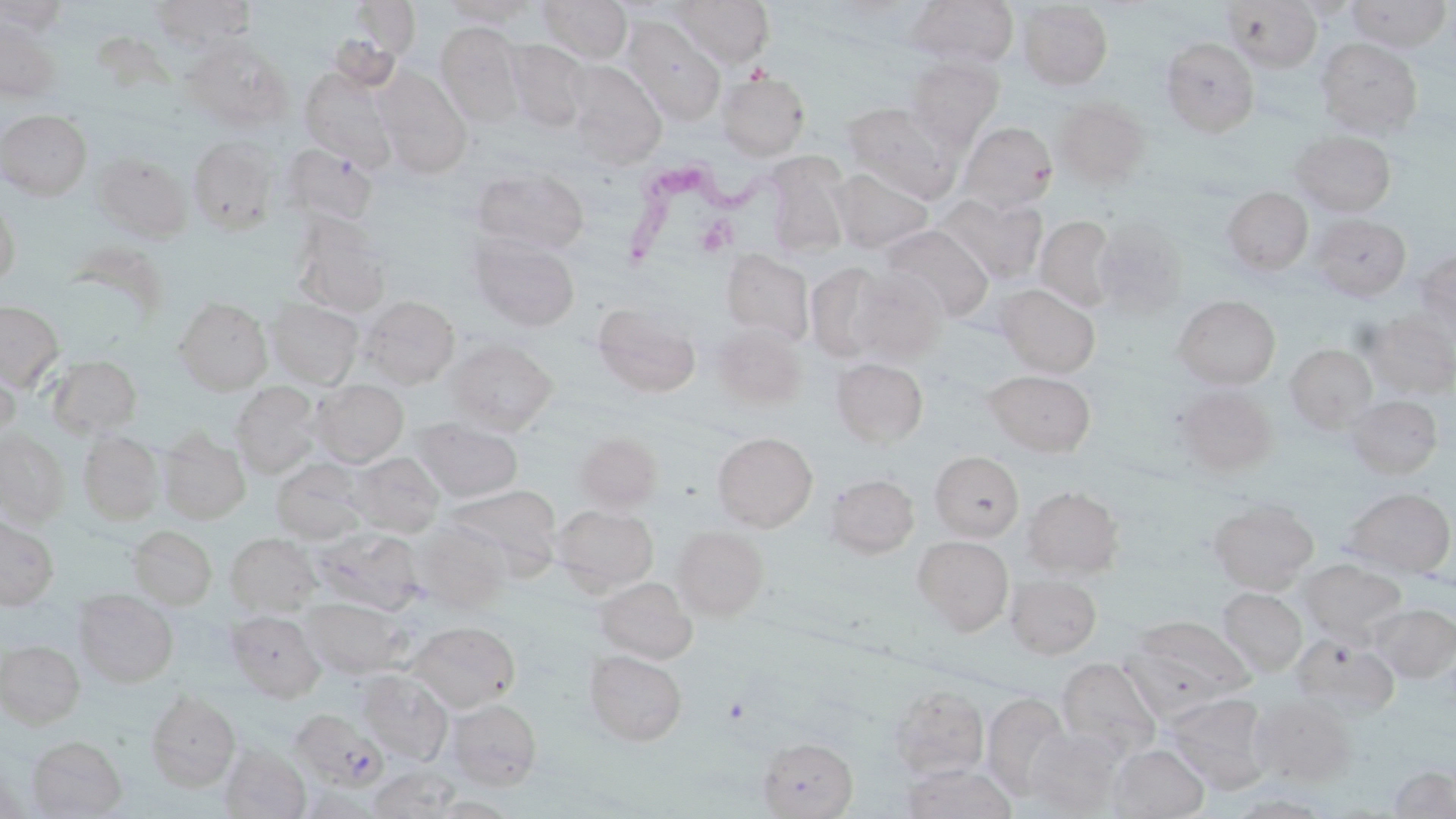
slide_level_diagnosis: Trypanosoma brucei
modality: light microscopy
image_size: 1456×819 pixels
trypanosoma_brucei_locations: 'approximate bounding boxes as (x1,y1)-(x2,y2) corner pairs in pixels: (622,156)-(792,274)'
magnification: 1000x
preparation: thin blood film
field_of_view: one of a larger specimen
uninfected_red_blood_cell_locations: 'approximate bounding boxes as (x1,y1)-(x2,y2) corner pairs in pixels: (0,0)-(71,35), (151,0)-(258,50), (348,0)-(421,60), (441,0)-(542,27), (536,0)-(632,64), (669,0)-(774,67), (909,0)-(1019,69), (1345,0)-(1453,51), (1221,1)-(1323,72), (1017,2)-(1113,90), (622,17)-(726,126), (0,21)-(62,102), (435,23)-(526,126), (1159,37)-(1260,137), (1315,38)-(1422,138), (505,39)-(590,131), (184,40)-(292,131), (904,58)-(1003,147), (565,60)-(668,167), (299,67)-(396,167), (373,67)-(472,177), (716,71)-(811,160), (1053,98)-(1151,188), (842,102)-(959,200), (0,110)-(92,200), (959,121)-(1058,211), (1290,130)-(1397,217), (187,136)-(279,233), (279,144)-(377,226), (92,153)-(192,242), (766,155)-(851,259), (469,167)-(589,256), (831,168)-(934,253), (1222,186)-(1313,276), (940,192)-(1047,284), (0,194)-(20,288), (1309,213)-(1411,302), (289,215)-(391,317), (1035,216)-(1118,314), (1092,220)-(1188,318), (880,224)-(993,321), (467,233)-(581,332), (82,246)-(168,326), (720,248)-(814,346), (1415,248)-(1456,335), (804,262)-(892,363), (849,269)-(949,364), (843,272)-(937,449), (996,284)-(1100,377), (359,295)-(460,388), (1173,295)-(1280,390), (174,298)-(272,394), (0,299)-(64,391), (266,299)-(363,387), (591,302)-(701,397), (1365,313)-(1456,399), (712,323)-(807,410), (446,338)-(557,433), (1286,344)-(1377,432), (47,354)-(142,439), (831,358)-(928,448), (0,361)-(19,444), (984,370)-(1096,457), (312,380)-(408,466), (230,382)-(322,477), (1173,386)-(1277,477), (1345,394)-(1443,479), (413,418)-(524,502), (0,431)-(70,525), (78,431)-(163,524), (158,431)-(251,524), (713,431)-(817,531), (575,433)-(663,511), (348,451)-(444,537), (929,451)-(1024,541), (271,459)-(369,543), (824,473)-(920,558), (445,484)-(561,573), (1022,486)-(1124,577), (1343,487)-(1456,577), (1208,498)-(1318,594), (552,504)-(659,592), (0,515)-(59,610), (410,522)-(511,612), (127,525)-(217,609), (671,525)-(770,620), (312,527)-(423,615), (226,533)-(320,614), (913,535)-(1014,634), (1300,559)-(1406,644), (1006,574)-(1101,659), (593,577)-(696,664), (1218,587)-(1307,675), (73,589)-(178,687), (303,598)-(407,677), (1372,603)-(1456,682), (226,610)-(326,701), (1124,616)-(1254,711), (409,621)-(519,712), (1291,635)-(1398,719), (0,640)-(85,728), (584,649)-(687,746), (1057,658)-(1159,755), (357,669)-(453,764), (887,685)-(988,780), (146,690)-(240,791), (982,693)-(1071,800), (1165,693)-(1274,794), (1250,694)-(1357,785), (446,699)-(542,789), (289,708)-(387,791), (1026,726)-(1126,816), (26,735)-(127,818), (758,737)-(857,818), (219,743)-(311,819), (1109,743)-(1209,818), (900,762)-(1019,819), (366,765)-(464,818), (1386,765)-(1456,817), (1226,792)-(1338,817), (427,795)-(521,818)'
stain: May-Grünwald-Giemsa